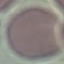
result = no malaria parasites seen
preparation = thin smear
image type = automatically extracted cell patch, resized to 64 × 64 pixels
capture = smartphone camera at the microscope eyepiece
stain = Giemsa